Identify the parasite.
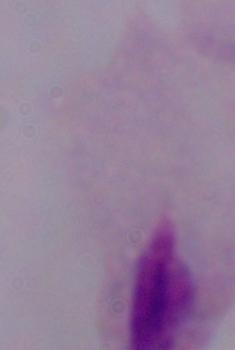
A trichomonad.

Summary:
  - Modality: micrograph
  - Magnification: 1000x